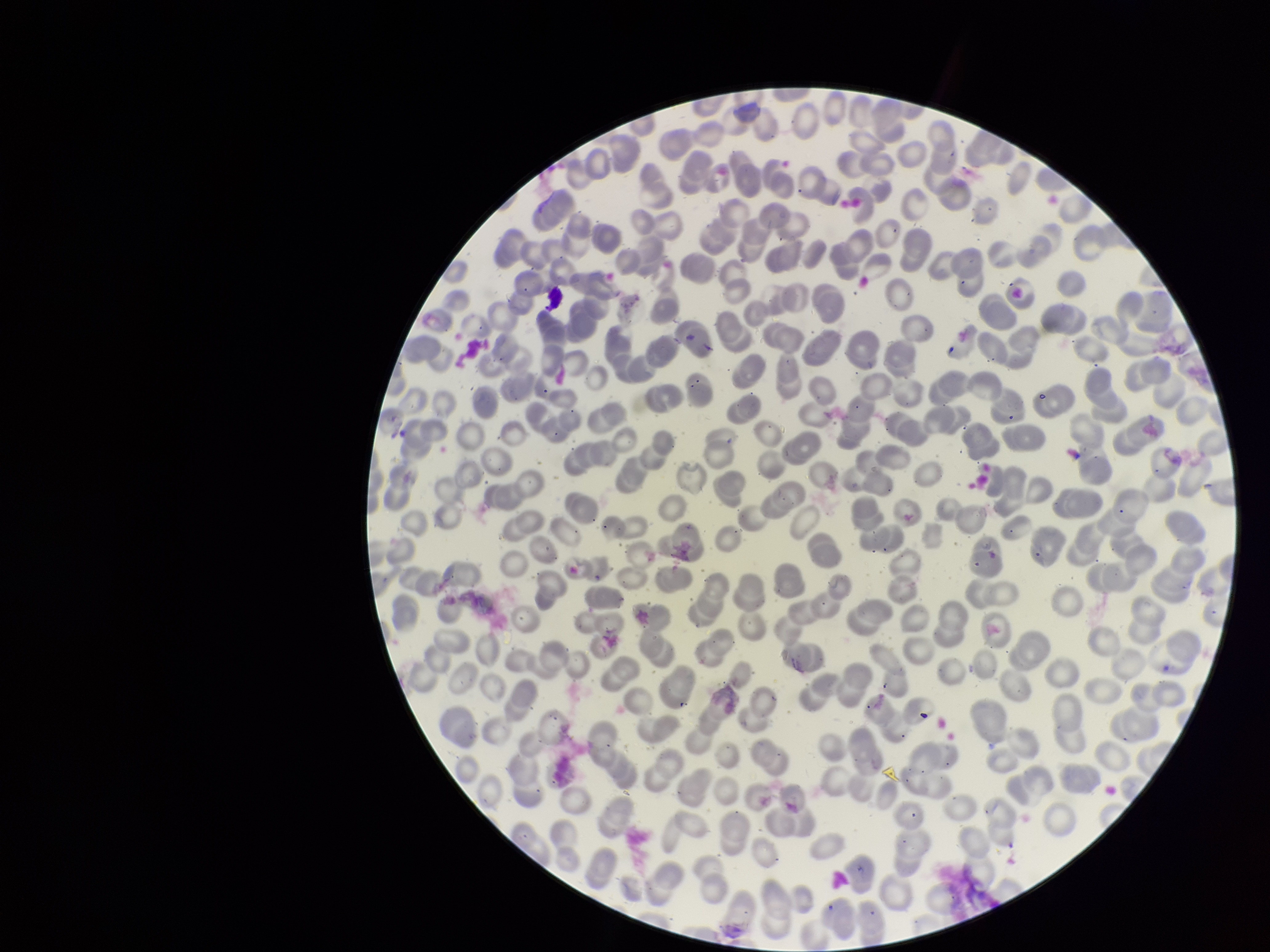 Image is 1270×952 pixels. Parasitized red blood cell count: 0. Patient malaria status: negative. Preparation: thin. Parasitized red blood cells: none seen. Photographed through the microscope eyepiece with a smartphone camera. Red blood cell count: 291. Giemsa stain. One field from this slide.